Report the malaria status of this cell.
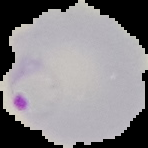
Parasitized.

Summary:
  - Image size: 148×148 pixels
  - Preparation: thin blood film
  - Image type: cell region segmented out of the field of view; surrounding area masked to black